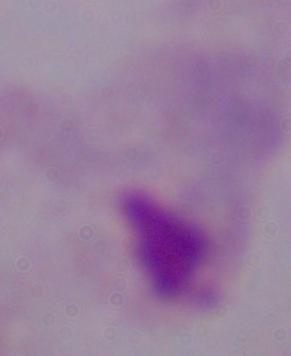
modality = photomicrograph
magnification = 1000x
identification = trichomonad